Classify this cell by malaria status.
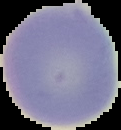
It is uninfected.

preparation = thin blood film
image type = segmented cell region on a black background
image size = 121×130 pixels